Identify the parasite.
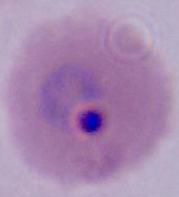
Plasmodium.

{
  "magnification": "400x or 1000x",
  "modality": "micrograph"
}